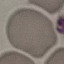

Summary:
  - Result: no malaria parasites detected
  - Preparation: thin blood smear
  - Image type: automatically extracted cell patch, resized to 64 × 64 pixels
  - Stain: Giemsa
  - Capture: smartphone camera at the microscope eyepiece